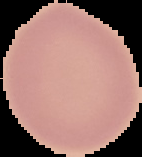
preparation = thin blood smear
image type = segmented cell region with the area outside set to black
result = negative for malaria parasites
image size = 142×157 pixels